Identify the blood parasite species.
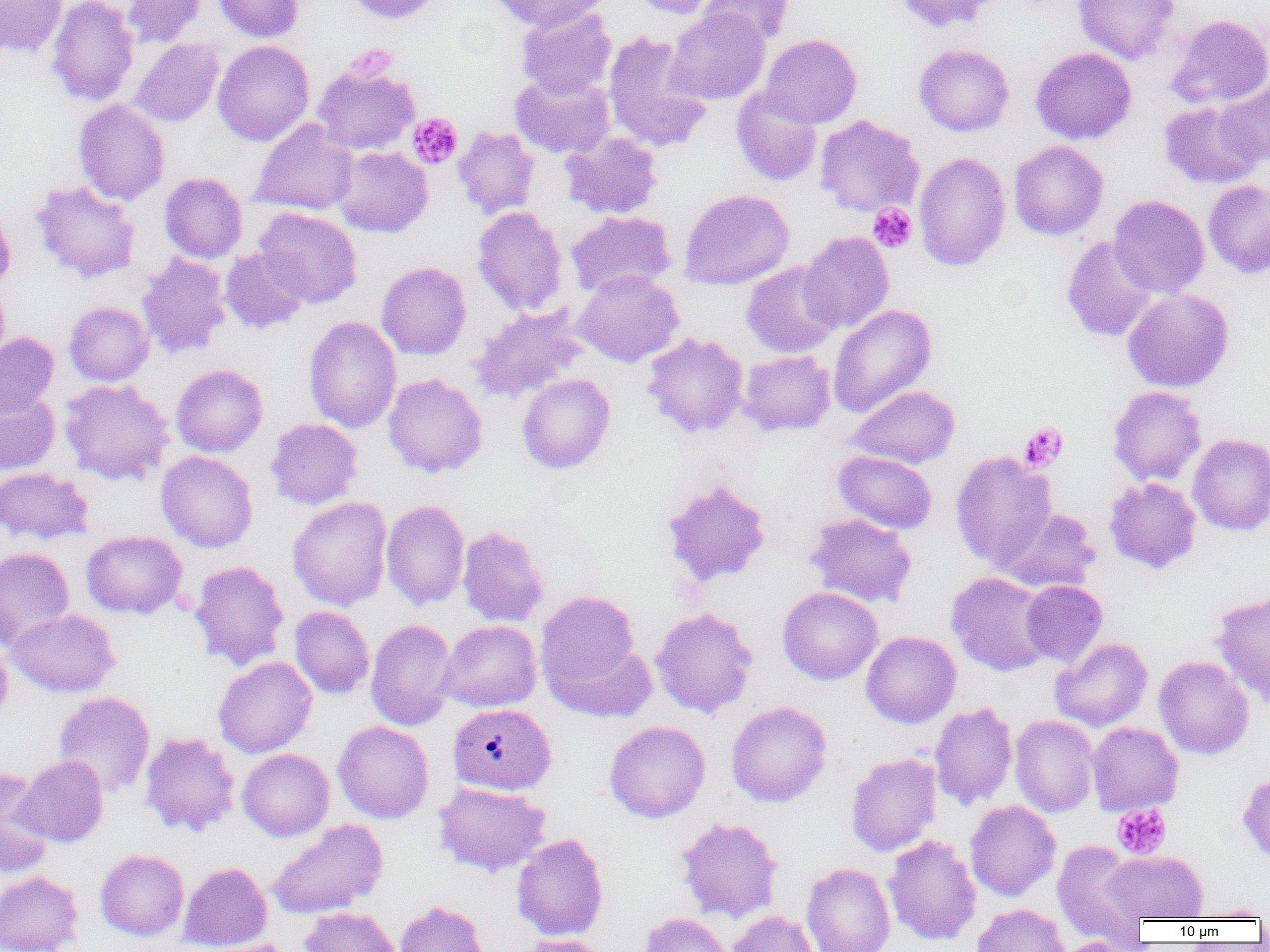

Plasmodium vivax.

uninfected red blood cell locations = approximate bounding boxes as (x1, y1, x2, y2) in pixels: (0, 0, 68, 57), (46, 0, 139, 107), (122, 0, 206, 47), (212, 0, 304, 41), (346, 0, 444, 25), (487, 0, 609, 31), (628, 0, 724, 19), (697, 0, 794, 47), (894, 0, 1000, 34), (1073, 0, 1180, 64), (517, 6, 616, 100), (664, 8, 770, 105), (1165, 13, 1270, 110), (602, 32, 711, 153), (761, 34, 862, 129), (130, 38, 224, 127), (212, 40, 315, 146), (913, 43, 1014, 136), (1030, 47, 1137, 144), (311, 62, 421, 155), (509, 72, 614, 159), (1215, 78, 1270, 165), (731, 86, 823, 187), (73, 100, 169, 205), (1158, 100, 1264, 190), (815, 115, 925, 217), (251, 118, 359, 215), (452, 126, 541, 220), (560, 132, 663, 219), (1008, 140, 1109, 240), (333, 146, 433, 238), (914, 152, 1011, 271), (159, 172, 247, 263), (30, 180, 141, 283), (1203, 180, 1270, 279), (679, 188, 794, 290), (1108, 195, 1210, 298), (0, 203, 15, 293), (472, 206, 567, 316), (253, 207, 362, 309), (566, 211, 676, 298), (800, 231, 894, 333), (1061, 236, 1159, 342), (220, 247, 310, 335), (136, 252, 232, 359), (376, 261, 471, 360), (741, 261, 842, 358), (573, 269, 684, 367), (0, 281, 10, 369), (1122, 288, 1234, 392), (64, 301, 154, 386), (828, 304, 936, 417), (468, 306, 588, 403), (303, 316, 402, 432), (0, 332, 59, 417), (642, 332, 749, 438), (738, 350, 835, 436), (171, 364, 268, 457), (383, 372, 488, 478), (517, 373, 615, 474), (59, 378, 174, 486), (847, 385, 960, 469), (1108, 386, 1207, 487), (0, 388, 60, 475), (265, 418, 363, 510), (1188, 433, 1270, 535), (156, 450, 258, 552), (833, 450, 937, 534), (951, 450, 1057, 571), (0, 467, 93, 545), (662, 477, 772, 589), (1104, 477, 1201, 573), (288, 496, 392, 611), (381, 499, 470, 611), (997, 507, 1101, 593), (804, 513, 917, 607), (457, 525, 549, 628), (81, 530, 187, 619), (0, 547, 75, 650), (189, 560, 290, 671), (946, 571, 1053, 676), (1021, 580, 1107, 666), (777, 587, 883, 685), (536, 591, 641, 694), (1212, 591, 1270, 709), (289, 606, 374, 698), (650, 606, 758, 718), (6, 608, 119, 697), (365, 618, 457, 731), (437, 620, 541, 712), (861, 631, 961, 728), (1051, 637, 1153, 731), (546, 639, 657, 722), (0, 641, 13, 722), (1154, 655, 1254, 759), (213, 656, 317, 758), (52, 692, 155, 797), (726, 700, 832, 808), (929, 701, 1018, 811), (1010, 714, 1099, 817), (332, 720, 434, 823), (604, 720, 711, 823), (1087, 722, 1183, 816), (139, 731, 240, 837), (237, 748, 334, 841), (845, 753, 942, 856), (13, 755, 108, 847), (0, 767, 53, 876), (1238, 771, 1270, 866), (433, 781, 551, 877), (964, 800, 1061, 901), (675, 816, 784, 922), (267, 818, 388, 920), (511, 832, 608, 941), (882, 834, 981, 946), (1052, 840, 1150, 943), (95, 849, 189, 941), (1104, 850, 1208, 923), (178, 862, 272, 951), (801, 862, 896, 952), (0, 870, 84, 952), (394, 899, 490, 952), (1191, 903, 1270, 921), (971, 904, 1072, 952), (300, 907, 401, 952), (726, 910, 818, 952), (638, 912, 732, 952), (518, 934, 612, 952), (1056, 937, 1142, 952), (193, 938, 295, 952)
preparation = thin blood smear
magnification = 1000x
modality = optical microscopy
image size = 1270×952 pixels
platelet locations = approximate bounding boxes as (x1, y1, x2, y2) in pixels: (345, 45, 397, 81), (407, 112, 463, 169), (868, 203, 917, 253), (1020, 422, 1068, 471), (1112, 803, 1171, 860)
field of view = single
Plasmodium vivax-infected red blood cell locations = approximate bounding boxes as (x1, y1, x2, y2) in pixels: (447, 703, 556, 795)